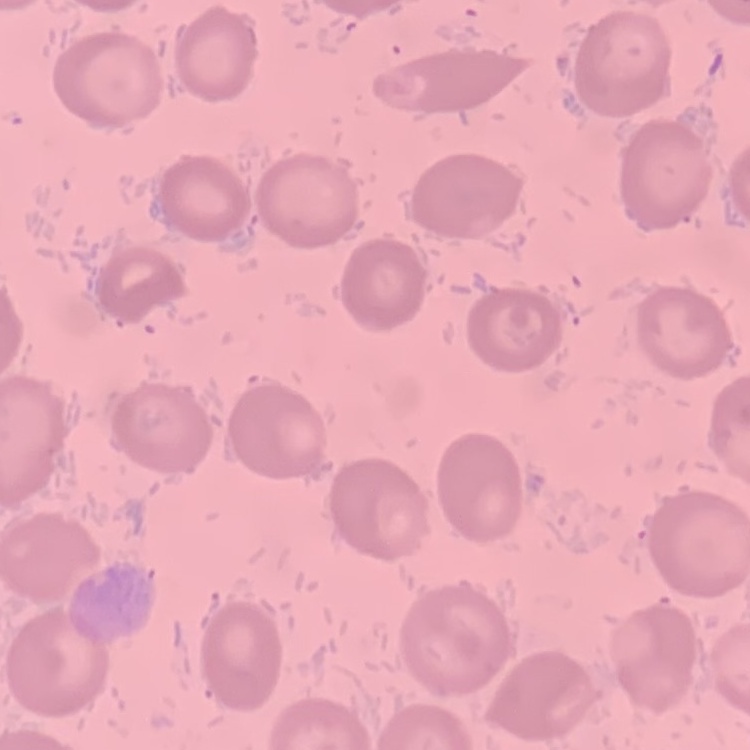 The erythrocytes show no rouleaux formation. One tile cut from a larger photomicrograph. Thin peripheral smear. Field's or Giemsa stain.